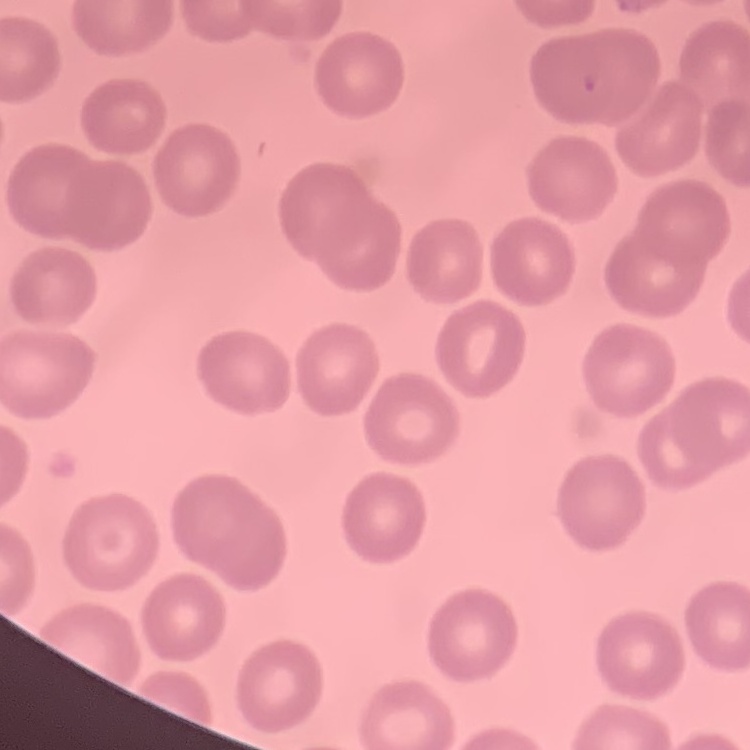
The erythrocytes show no rouleaux formation. Thin blood smear. One tile cut from a larger photomicrograph. Field's or Giemsa stain.